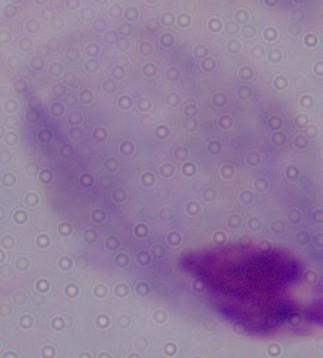

Captured at 1000x magnification. Photomicrograph. A trichomonad is seen.